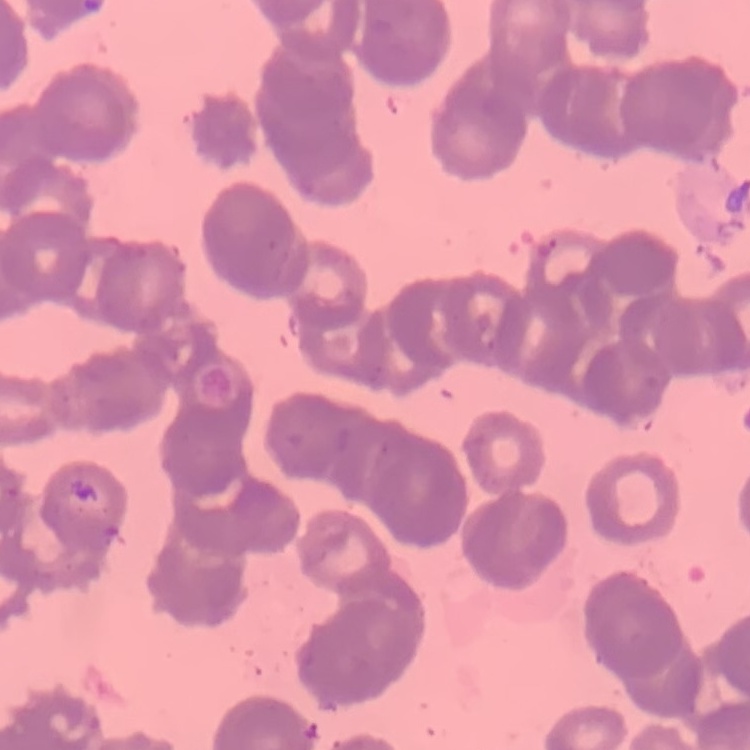

The erythrocytes exhibit rouleaux formation. Thin peripheral smear. Square crop of a larger photomicrograph. Stained with either Field's or Giemsa.